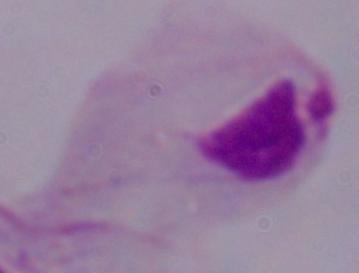

modality = photomicrograph
magnification = 1000x
identification = trichomonad